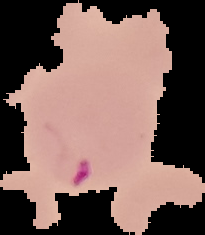

Cell region segmented out of the field of view; the surrounding area is masked to black. Result: Plasmodium parasites identified. From a thin blood smear. Image is 205×235 pixels.